Locate every blood parasite and identify its species.
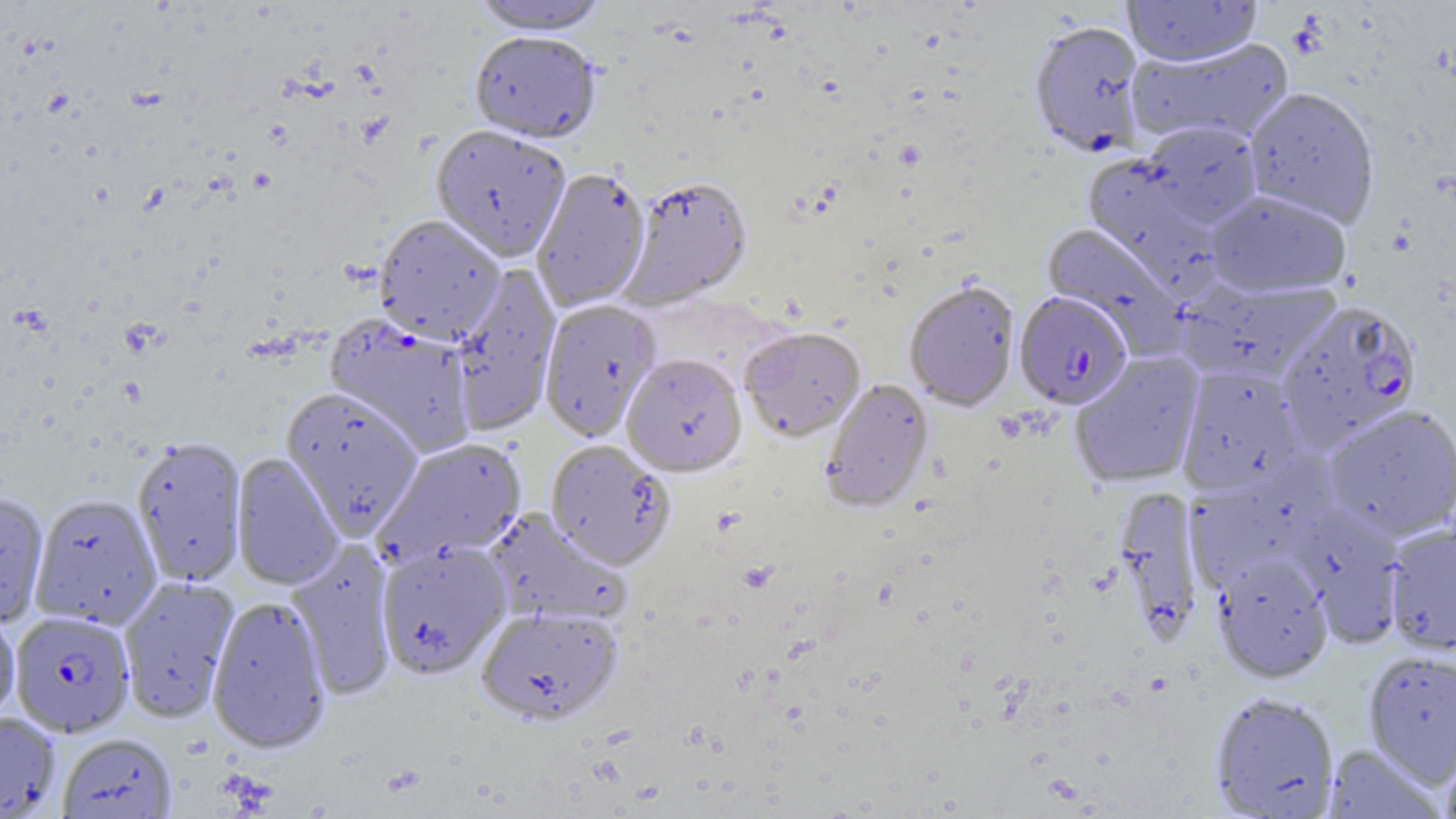
Approximate bounding boxes as (x1,y1)-(x2,y2) corner pairs in pixels.
Plasmodium falciparum-infected red blood cells: (1014,292)-(1132,409), (1275,300)-(1422,449), (9,611)-(134,737).
No Plasmodium ovale, Plasmodium malariae, Plasmodium vivax, Babesia divergens, or Trypanosoma brucei observed.

Uninfected red blood cell locations: (470,0)-(611,35), (1123,0)-(1261,67), (1028,20)-(1148,158), (469,32)-(601,144), (1127,38)-(1294,147), (1243,87)-(1381,227), (1142,120)-(1263,227), (430,125)-(571,261), (1083,154)-(1221,288), (531,167)-(650,312), (619,175)-(753,309), (1205,189)-(1352,298), (373,214)-(506,345), (1041,222)-(1185,353), (449,264)-(561,436), (1179,279)-(1342,382), (904,280)-(1020,411), (538,299)-(662,442), (325,316)-(477,456), (740,327)-(866,442), (1070,352)-(1204,488), (621,353)-(747,477), (1178,364)-(1306,494), (820,378)-(934,512), (281,387)-(423,538), (1322,404)-(1456,541), (132,436)-(247,587), (374,438)-(527,567), (545,440)-(676,570), (231,453)-(343,590), (1184,465)-(1326,592), (1113,485)-(1203,643), (0,492)-(51,628), (29,493)-(162,630), (1291,505)-(1406,645), (483,508)-(631,627), (1384,524)-(1456,655), (375,539)-(512,679), (286,542)-(397,699), (1213,553)-(1334,683), (118,576)-(239,723), (207,596)-(332,754), (477,606)-(622,726), (0,610)-(20,723), (1363,651)-(1456,785), (1210,692)-(1340,818), (0,711)-(61,819), (57,733)-(178,819), (1440,734)-(1456,819), (1324,744)-(1444,818). Slide-level diagnosis: Plasmodium falciparum. 1000x magnification. Image is 1456×819 pixels. Single field of view. Thin blood smear. Optical microscopy.